Locate every Babesia divergens-infected red blood cell.
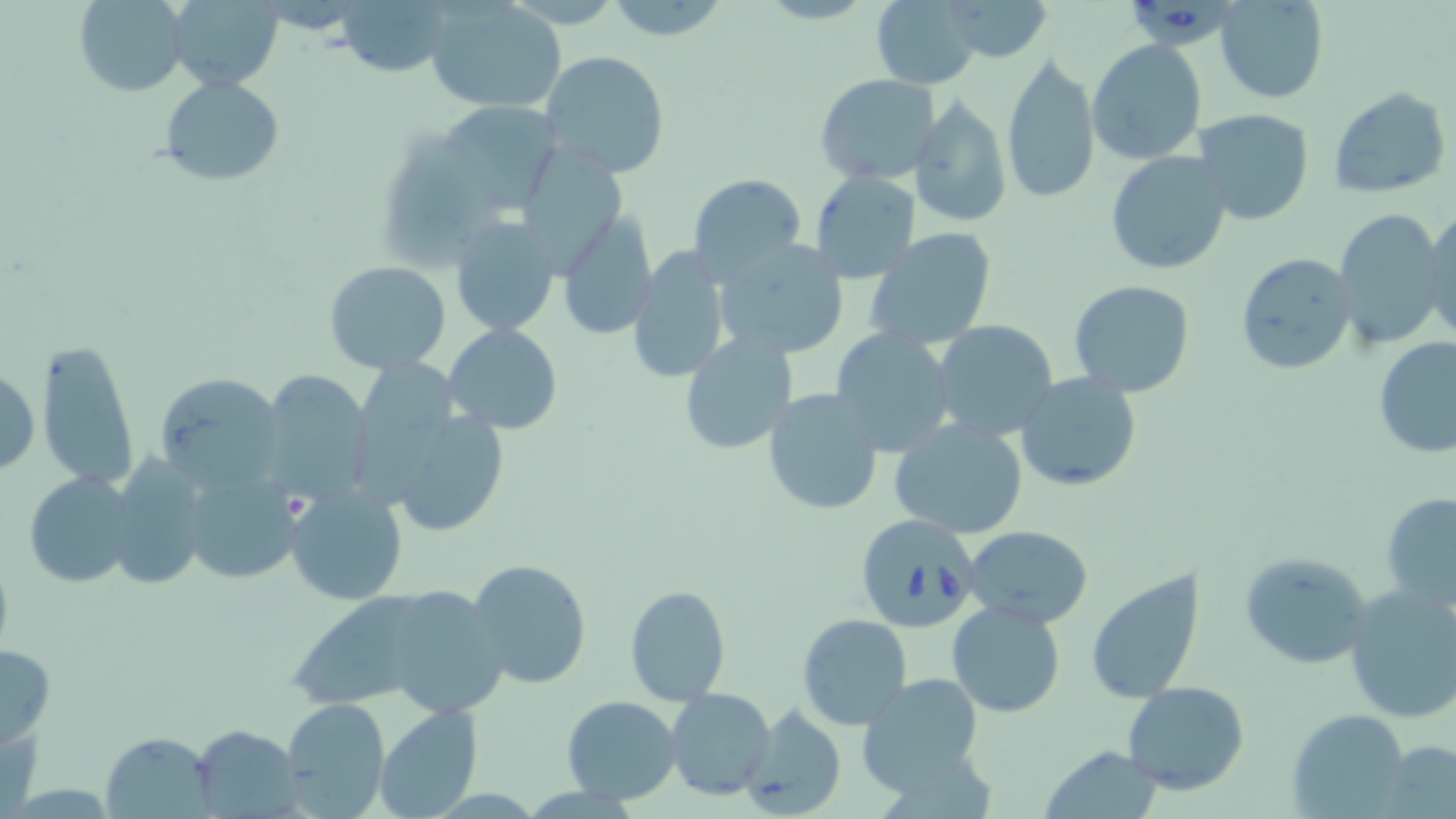

Approximate bounding boxes as (x1, y1, x2, y2) in pixels.
Babesia divergens-infected red blood cells: (1131, 0, 1222, 52), (852, 512, 983, 633).

Summary:
  - Uninfected red blood cell locations: (74, 0, 190, 97), (344, 0, 457, 80), (1214, 0, 1328, 103), (167, 1, 285, 86), (603, 1, 734, 44), (870, 1, 984, 89), (940, 1, 1053, 64), (427, 2, 566, 116), (1087, 39, 1207, 165), (539, 51, 670, 179), (1000, 52, 1101, 205), (814, 74, 941, 185), (157, 75, 286, 187), (1329, 86, 1451, 198), (907, 96, 1011, 229), (442, 99, 558, 214), (1192, 108, 1316, 228), (526, 148, 621, 276), (1105, 151, 1233, 275), (808, 170, 923, 284), (688, 173, 807, 282), (1333, 206, 1448, 350), (1421, 206, 1456, 342), (556, 215, 657, 341), (448, 216, 560, 337), (865, 228, 998, 350), (714, 239, 850, 362), (626, 247, 730, 385), (1235, 252, 1357, 375), (323, 262, 452, 373), (1068, 279, 1197, 398), (930, 320, 1059, 441), (444, 323, 562, 434), (832, 325, 957, 455), (677, 331, 800, 455), (1374, 337, 1456, 458), (37, 338, 139, 490), (0, 362, 40, 480), (257, 371, 371, 505), (154, 372, 291, 492), (1014, 372, 1144, 493), (762, 389, 884, 516), (370, 397, 515, 540), (888, 421, 1030, 538), (107, 455, 210, 593), (179, 463, 303, 587), (24, 470, 138, 588), (285, 484, 410, 605), (1380, 491, 1456, 613), (964, 526, 1094, 627), (1239, 551, 1373, 670), (466, 559, 592, 689), (1084, 569, 1204, 703), (623, 583, 731, 706), (1342, 584, 1456, 726), (946, 600, 1068, 719), (796, 614, 913, 731), (0, 642, 56, 747), (855, 672, 986, 794), (1121, 681, 1250, 795), (665, 688, 776, 801), (562, 695, 682, 805), (282, 699, 388, 816), (738, 704, 846, 819), (371, 705, 484, 818), (1288, 708, 1409, 819), (189, 726, 303, 818), (101, 732, 216, 818), (1380, 741, 1456, 818), (1041, 745, 1163, 819)
  - Slide-level diagnosis: Babesia divergens
  - Image size: 1456×819 pixels
  - Preparation: thin blood film
  - Stain: May-Grünwald-Giemsa
  - Modality: optical microscopy
  - Magnification: 1000x
  - Field of view: single